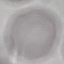

result = negative for malaria parasites
stain = Giemsa
image type = cell patch, automatically extracted from a larger field of view and resized to 64 × 64 pixels
capture = smartphone camera at the microscope eyepiece
preparation = thin blood smear